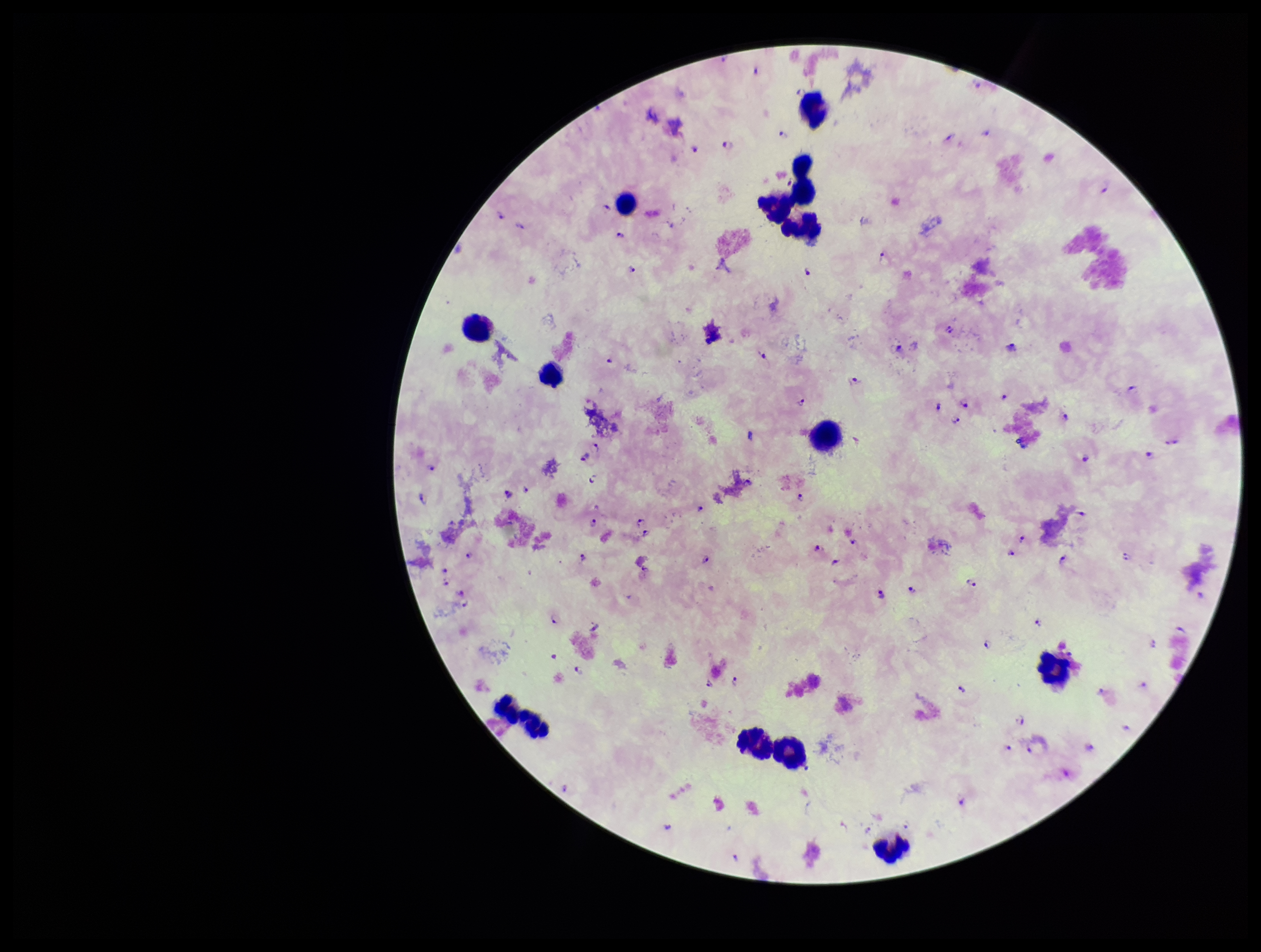
preparation = thick smear
species reported for this patient = Plasmodium falciparum
patient malaria status = positive
leukocyte count = 14
field of view = single
image size = 1261×952 pixels
stain = Giemsa
capture = smartphone photograph through the microscope eyepiece
Plasmodium parasites = seen
parasite count = 109